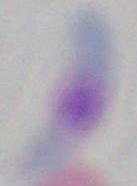
Summary:
  - Modality: photomicrograph
  - Identification: Toxoplasma gondii
  - Magnification: 1000x